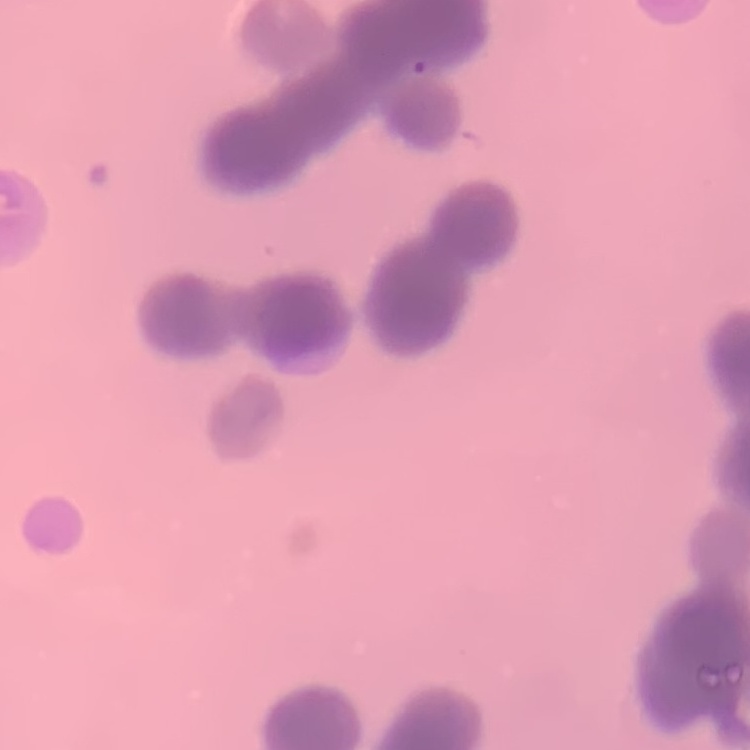

{
  "red_blood_cell_morphology": "rouleaux formation",
  "image_type": "square crop of a larger photomicrograph",
  "stain": "Field's or Giemsa",
  "preparation": "thin blood smear"
}